Identify the parasite.
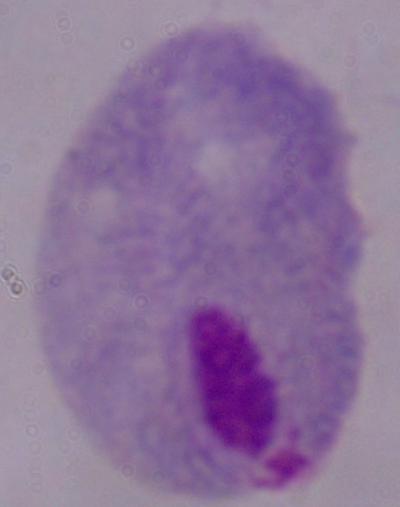

A trichomonad.

modality: micrograph
magnification: 1000x